Name the cell type shown.
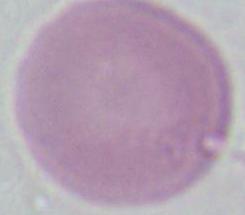
This is an erythrocyte.

1000x magnification. Photomicrograph.